Assess the morphology of the erythrocytes.
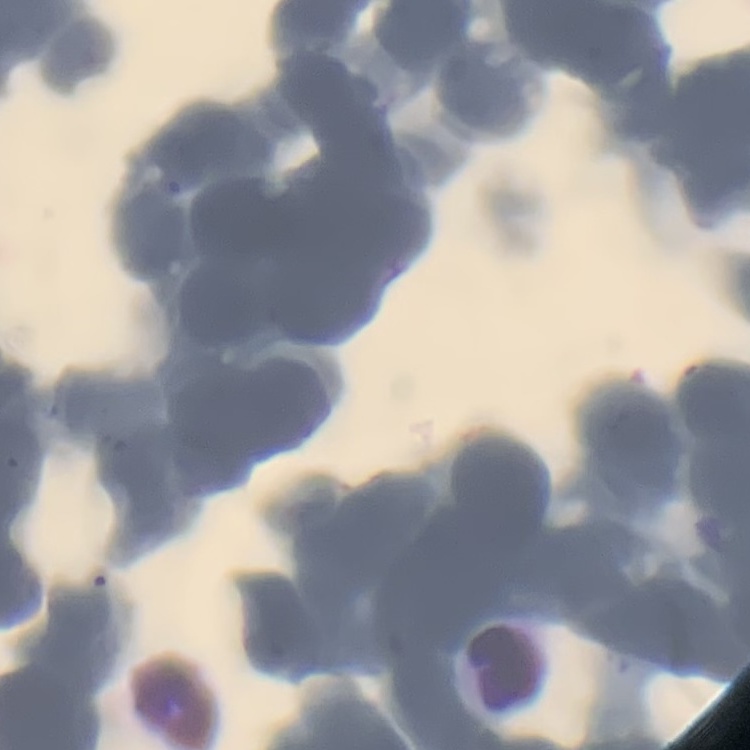
Rouleaux formation.

Summary:
  - Stain: Field's or Giemsa
  - Preparation: thin peripheral smear
  - Image type: one tile cut from a larger photomicrograph